Classify this cell by malaria status.
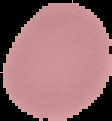

It is uninfected.

Summary:
  - Preparation: thin blood film
  - Image type: segmented cell region on a black background
  - Image size: 112×121 pixels